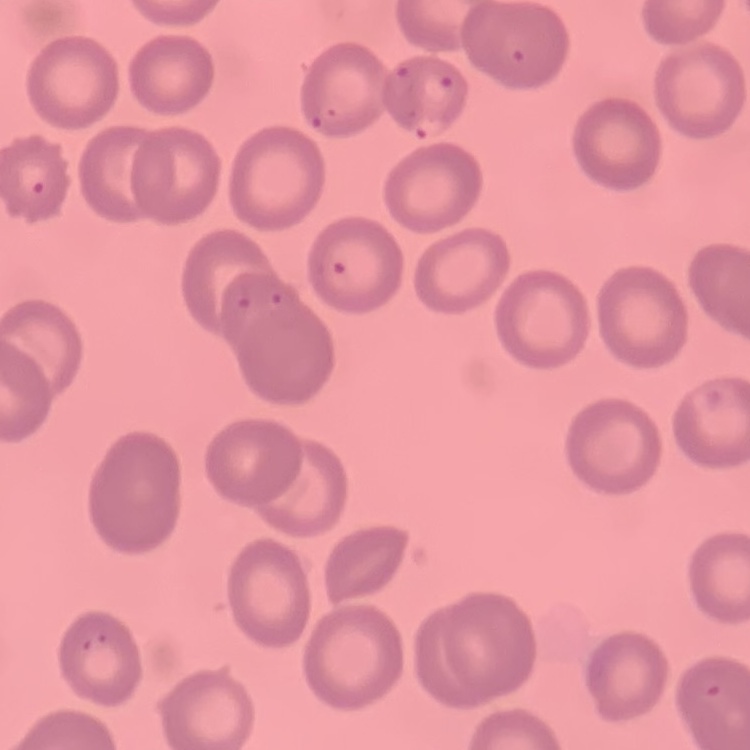
red blood cell morphology = no rouleaux formation
image type = one tile cut from a larger photomicrograph
preparation = thin blood film
stain = Field's or Giemsa